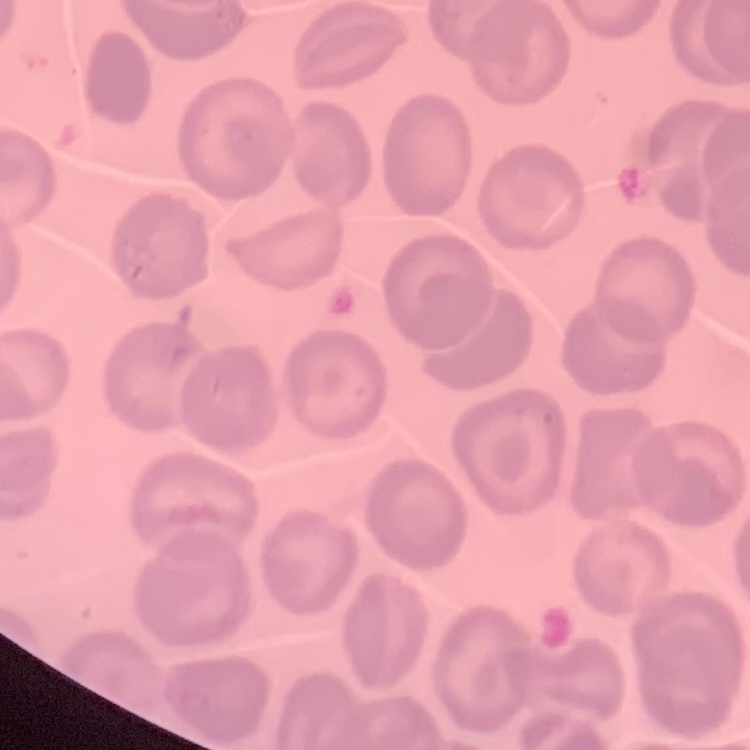
red_blood_cell_morphology: no rouleaux formation
preparation: thin blood smear
stain: Field's or Giemsa
image_type: one tile cut from a larger photomicrograph